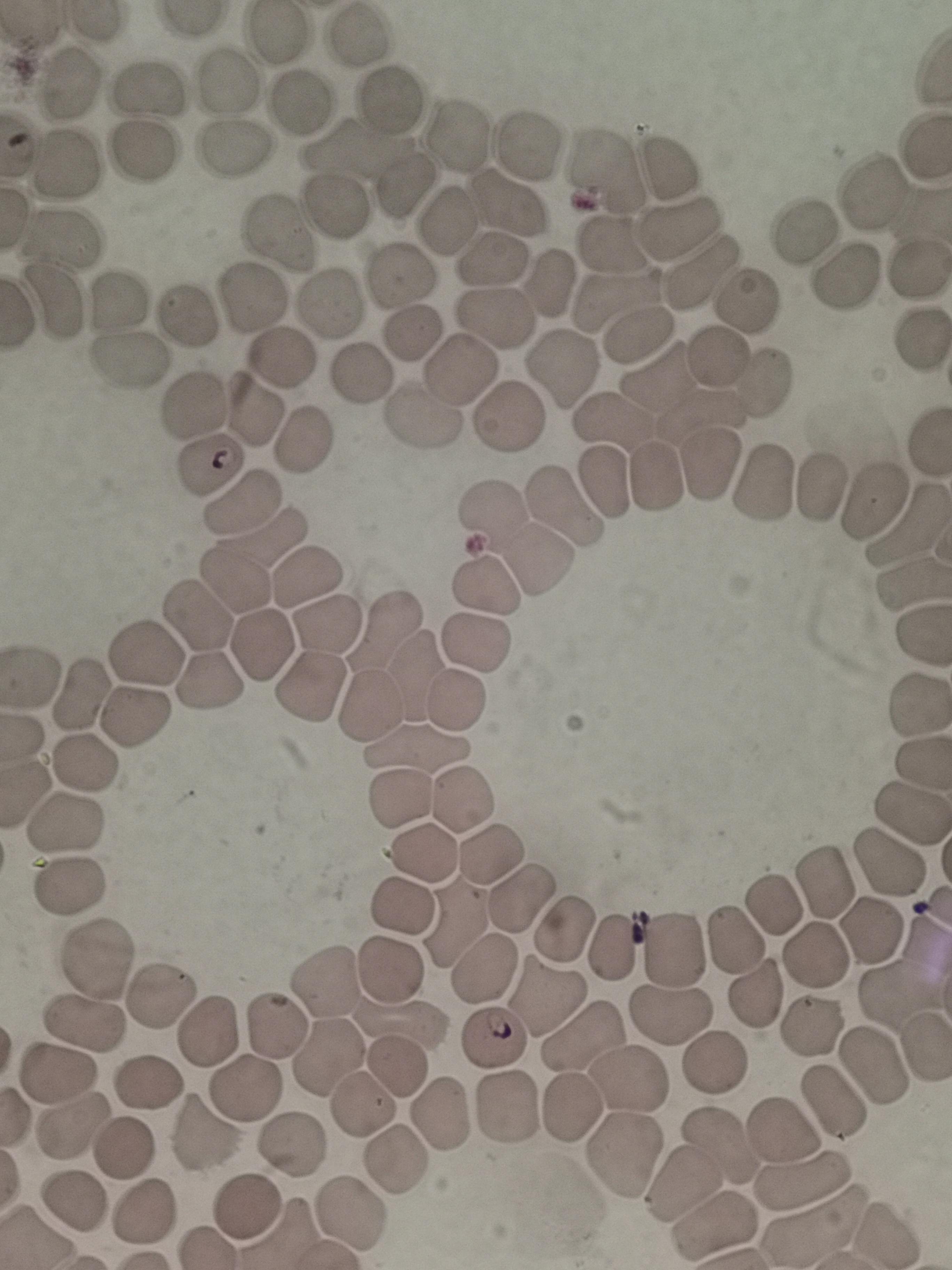

Approximate centers as (x, y) in pixels.
Summary:
  - Cell locations: (360, 43), (66, 89), (223, 89), (153, 90), (392, 98), (301, 101), (459, 135), (534, 141), (234, 150), (139, 151), (61, 165), (605, 167), (668, 169), (402, 185), (870, 197), (509, 201), (329, 217), (447, 217), (280, 230), (681, 230), (60, 234), (799, 235), (612, 239), (491, 262), (918, 269), (699, 270), (400, 276), (843, 280), (551, 284), (250, 295), (617, 295), (749, 300), (57, 301), (110, 302), (325, 305), (496, 311), (185, 314), (411, 333), (636, 337), (917, 339), (280, 356), (719, 357), (128, 360), (565, 366), (457, 367), (366, 372), (656, 383), (761, 385), (192, 407), (504, 414), (617, 420), (707, 420), (414, 424), (301, 439), (713, 465), (207, 470), (655, 478), (607, 481), (761, 485), (818, 489), (870, 502), (241, 507), (564, 510), (493, 513), (907, 525), (266, 537), (538, 560), (305, 578), (231, 579), (484, 584), (198, 614), (326, 627), (384, 630), (262, 642), (476, 642), (142, 651), (415, 672), (213, 678), (310, 684), (81, 695), (457, 698), (920, 707), (372, 710), (137, 717), (417, 746), (87, 762), (405, 794), (461, 795), (908, 810), (66, 826), (493, 845), (422, 850), (888, 863), (830, 876), (74, 886), (520, 891), (776, 900), (404, 901), (456, 920), (566, 924), (868, 929), (735, 937), (609, 944), (676, 944), (814, 949), (96, 959), (483, 967), (386, 970), (325, 986), (158, 993), (758, 995), (546, 996), (668, 1015), (401, 1019), (83, 1024), (812, 1024), (272, 1025), (207, 1029), (496, 1036), (582, 1036), (324, 1056), (715, 1061), (397, 1067), (874, 1067), (59, 1076), (630, 1078), (149, 1084), (246, 1089), (833, 1102), (359, 1103), (574, 1106), (506, 1110), (441, 1111), (74, 1124), (785, 1129), (207, 1136), (291, 1147), (719, 1147), (622, 1149), (123, 1151), (398, 1157), (683, 1176), (803, 1182), (71, 1204), (250, 1207), (141, 1212), (356, 1212), (811, 1225), (716, 1228)
  - Image size: 952×1270 pixels
  - Field of view: single
  - Preparation: thin smear
  - Stain: Giemsa
  - Capture: smartphone camera at the microscope eyepiece